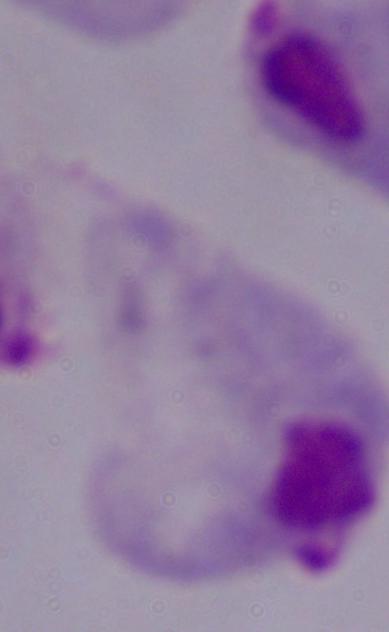
Captured at 1000x magnification. Micrograph. A trichomonad is seen.